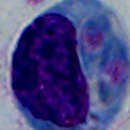

{
  "modality": "photomicrograph",
  "identification": "leukocyte",
  "magnification": "1000x"
}